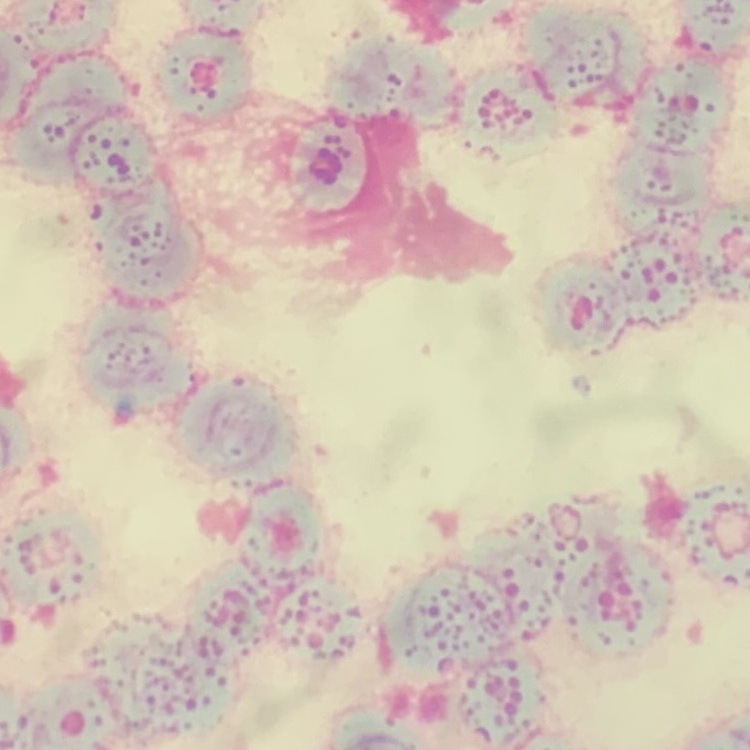

{
  "erythrocyte_morphology": "rouleaux formation",
  "image_type": "one tile cut from a larger photomicrograph",
  "preparation": "thin blood film",
  "stain": "Field's or Giemsa"
}